Evaluate for malaria.
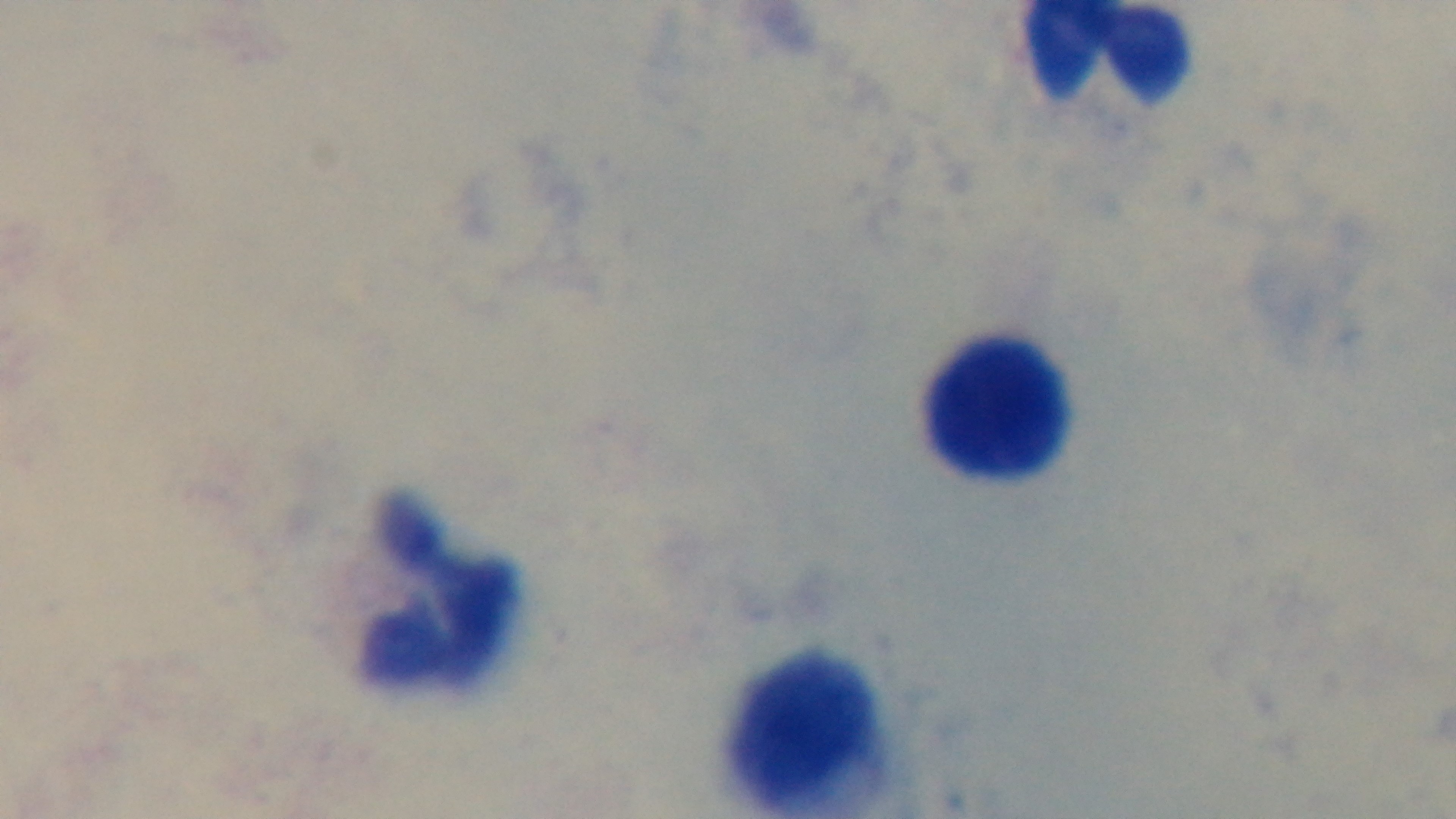
It is uninfected.

stain: Giemsa
field_of_view: single
modality: light microscopy
objective: 100x oil immersion
preparation: thick smear
capture: mounted 4K digital camera